Locate and identify every blood parasite.
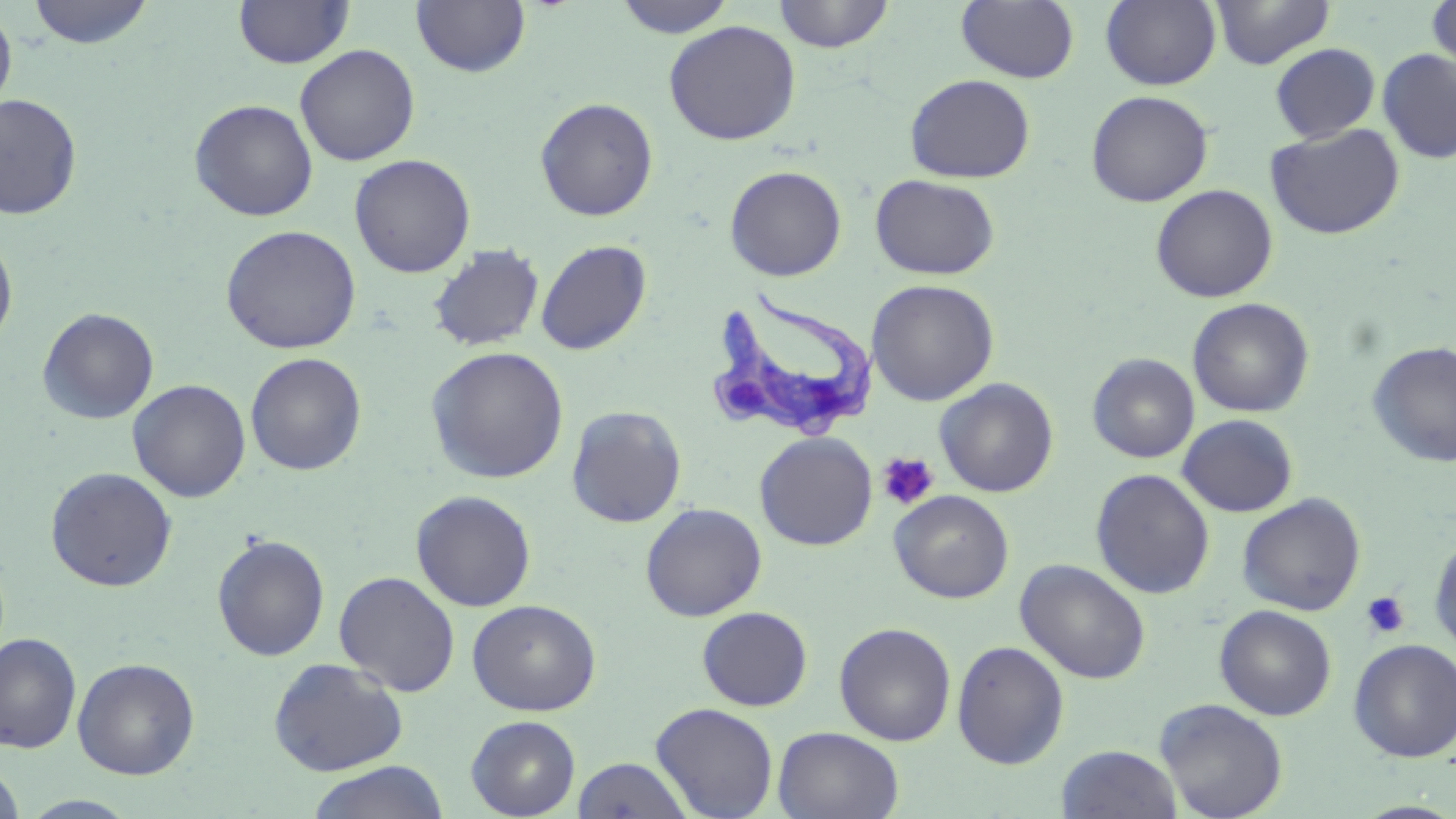
Approximate bounding boxes as named x1/y1/x2/y2 corners in pixels.
Trypanosoma brucei: (x1=706, y1=287, x2=880, y2=443).
No Plasmodium falciparum, Plasmodium ovale, Plasmodium malariae, Plasmodium vivax, or Babesia divergens observed.

Platelet locations: (x1=877, y1=452, x2=939, y2=511), (x1=1362, y1=591, x2=1410, y2=639). Uninfected red blood cell locations: (x1=26, y1=0, x2=154, y2=49), (x1=233, y1=0, x2=354, y2=69), (x1=613, y1=0, x2=736, y2=38), (x1=773, y1=0, x2=895, y2=53), (x1=957, y1=0, x2=1079, y2=84), (x1=1101, y1=0, x2=1222, y2=90), (x1=1210, y1=0, x2=1335, y2=69), (x1=1427, y1=0, x2=1456, y2=79), (x1=411, y1=1, x2=530, y2=78), (x1=0, y1=4, x2=17, y2=119), (x1=663, y1=20, x2=801, y2=145), (x1=1270, y1=43, x2=1380, y2=144), (x1=295, y1=44, x2=420, y2=167), (x1=1377, y1=49, x2=1456, y2=164), (x1=905, y1=73, x2=1036, y2=183), (x1=1086, y1=90, x2=1214, y2=208), (x1=0, y1=93, x2=82, y2=220), (x1=535, y1=97, x2=659, y2=221), (x1=189, y1=99, x2=318, y2=221), (x1=1265, y1=122, x2=1405, y2=241), (x1=349, y1=153, x2=476, y2=278), (x1=724, y1=165, x2=847, y2=281), (x1=871, y1=174, x2=1000, y2=280), (x1=1149, y1=184, x2=1278, y2=303), (x1=220, y1=225, x2=361, y2=354), (x1=0, y1=233, x2=18, y2=351), (x1=536, y1=239, x2=651, y2=355), (x1=428, y1=244, x2=545, y2=352), (x1=866, y1=279, x2=1000, y2=406), (x1=1187, y1=298, x2=1314, y2=418), (x1=37, y1=307, x2=159, y2=424), (x1=1368, y1=341, x2=1456, y2=468), (x1=425, y1=346, x2=569, y2=483), (x1=245, y1=352, x2=367, y2=475), (x1=1087, y1=353, x2=1200, y2=463), (x1=934, y1=378, x2=1059, y2=497), (x1=127, y1=379, x2=251, y2=502), (x1=566, y1=405, x2=687, y2=527), (x1=1177, y1=414, x2=1299, y2=517), (x1=754, y1=432, x2=877, y2=550), (x1=45, y1=466, x2=178, y2=592), (x1=1090, y1=468, x2=1215, y2=599), (x1=410, y1=489, x2=537, y2=612), (x1=889, y1=490, x2=1014, y2=603), (x1=1237, y1=494, x2=1366, y2=616), (x1=640, y1=502, x2=767, y2=621), (x1=1427, y1=528, x2=1456, y2=656), (x1=211, y1=533, x2=330, y2=661), (x1=1015, y1=558, x2=1151, y2=684), (x1=334, y1=571, x2=460, y2=696), (x1=467, y1=598, x2=601, y2=716), (x1=1214, y1=604, x2=1336, y2=721), (x1=697, y1=606, x2=813, y2=711), (x1=834, y1=622, x2=956, y2=746), (x1=0, y1=633, x2=82, y2=753), (x1=1349, y1=638, x2=1456, y2=762), (x1=952, y1=640, x2=1070, y2=769), (x1=268, y1=657, x2=409, y2=776), (x1=73, y1=658, x2=200, y2=780), (x1=1154, y1=697, x2=1289, y2=819), (x1=650, y1=702, x2=779, y2=819), (x1=466, y1=715, x2=581, y2=819), (x1=774, y1=726, x2=903, y2=819), (x1=1056, y1=745, x2=1183, y2=819), (x1=573, y1=756, x2=693, y2=819), (x1=305, y1=761, x2=450, y2=819), (x1=0, y1=764, x2=26, y2=819), (x1=18, y1=794, x2=141, y2=818). Slide-level diagnosis: Trypanosoma brucei. Image is 1456×819 pixels. Single field of view. May-Grünwald-Giemsa-stained preparation. 1000x magnification. Thin blood film. Optical microscopy.